Assess the morphology of the red blood cells.
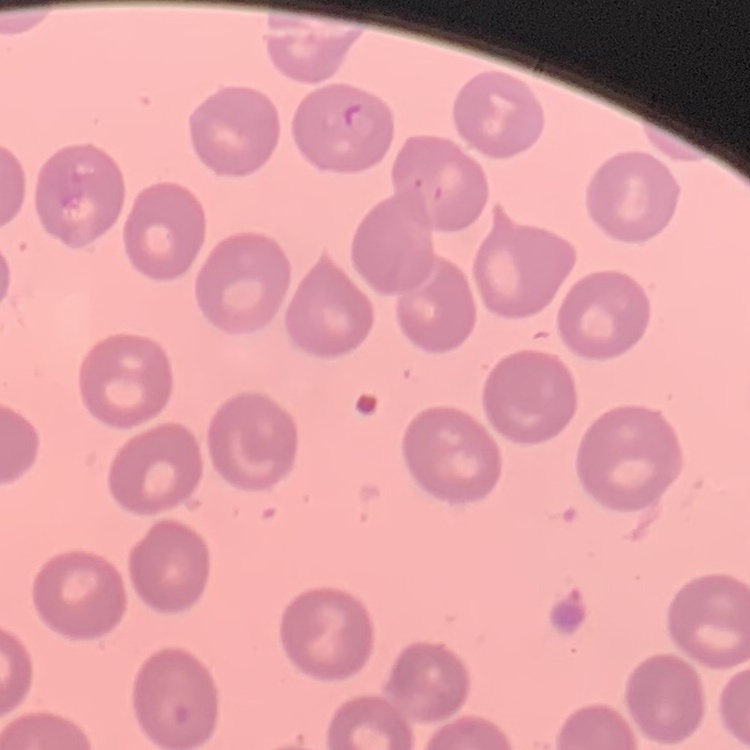

No rouleaux formation.

image_type: one tile cut from a larger photomicrograph
preparation: thin blood film
stain: Field's or Giemsa